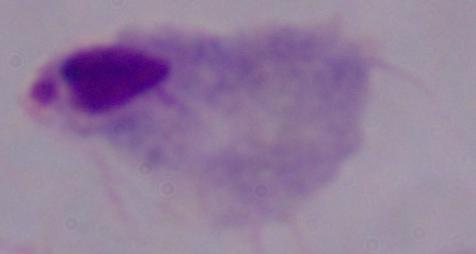

Summary:
  - Magnification: 1000x
  - Identification: trichomonad
  - Modality: photomicrograph